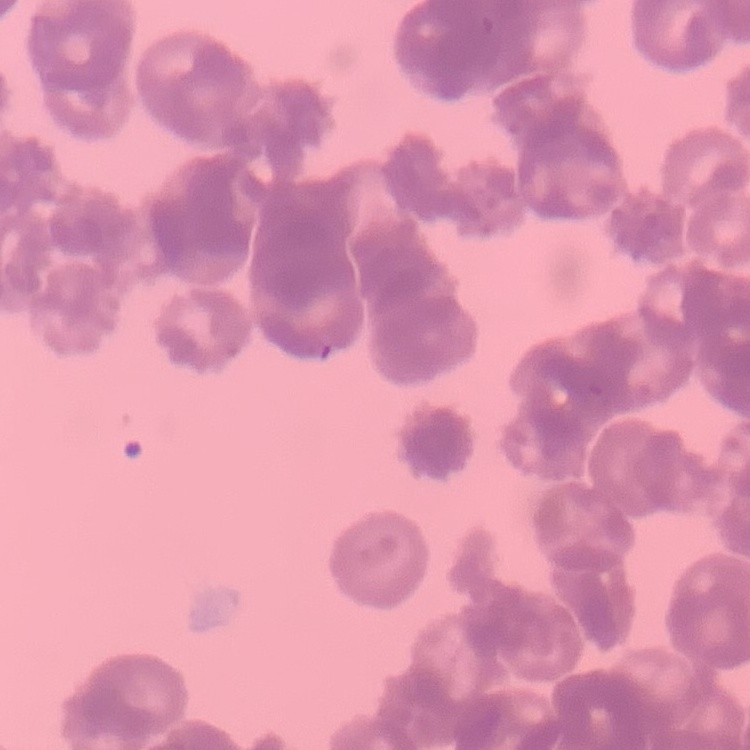
The erythrocytes show rouleaux formation. Stained with either Field's or Giemsa. Thin blood film. One tile cut from a larger photomicrograph.